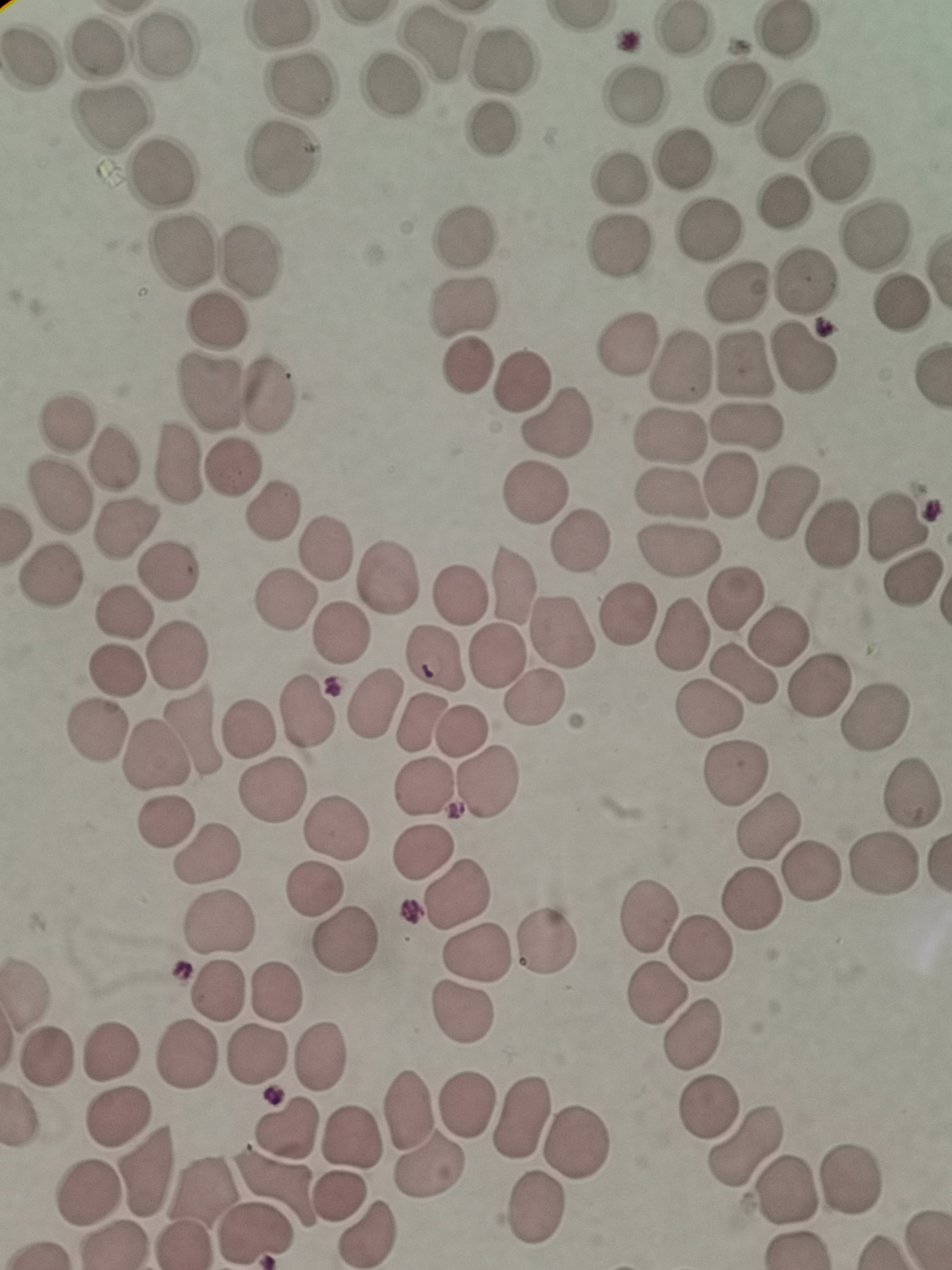

{
  "cell_locations": "approximate centers as (x, y) in pixels: (683, 31), (786, 31), (99, 44), (434, 44), (165, 45), (32, 57), (504, 59), (300, 83), (391, 91), (636, 93), (736, 93), (108, 120), (788, 121), (491, 127), (281, 158), (685, 158), (840, 169), (162, 171), (619, 179), (710, 230), (875, 236), (463, 237), (620, 245), (181, 251), (251, 260), (806, 280), (738, 290), (462, 305), (901, 305), (219, 319), (626, 344), (804, 358), (743, 365), (468, 366), (682, 366), (518, 381), (270, 394), (208, 395), (66, 421), (558, 423), (746, 426), (669, 434), (115, 459), (179, 465), (233, 470), (731, 481), (59, 495), (532, 495), (669, 495), (788, 505), (272, 514), (898, 526), (126, 530), (833, 536), (579, 541), (326, 547), (677, 552), (167, 569), (48, 577), (388, 577), (912, 580), (512, 582), (461, 593), (734, 598), (283, 599), (120, 613), (632, 613), (562, 632), (778, 634), (339, 635), (683, 637), (175, 654), (498, 655), (436, 656), (115, 670), (745, 677), (819, 685), (534, 697), (376, 699), (307, 711), (707, 711), (877, 718), (416, 723), (249, 727), (195, 729), (461, 729), (95, 731), (154, 757), (734, 775), (488, 781), (422, 786), (270, 789), (910, 793), (166, 820), (338, 828), (769, 829), (422, 852), (205, 856), (884, 864), (814, 872), (312, 890), (458, 894), (647, 913), (220, 925), (345, 941), (546, 942), (696, 948), (475, 952), (216, 990), (274, 992), (656, 994), (462, 1012), (695, 1037), (111, 1053), (45, 1055), (186, 1055), (257, 1055), (320, 1057), (465, 1106), (710, 1107), (409, 1111), (118, 1119), (520, 1119), (286, 1126), (349, 1138), (579, 1145), (747, 1146), (430, 1165), (144, 1171), (850, 1179), (274, 1188), (200, 1189), (787, 1190), (87, 1193), (340, 1196), (537, 1208), (366, 1235), (253, 1236), (113, 1243), (182, 1246)",
  "stain": "Giemsa",
  "image_size": "952×1270 pixels",
  "field_of_view": "single",
  "preparation": "thin blood smear",
  "capture": "smartphone through the microscope eyepiece"
}